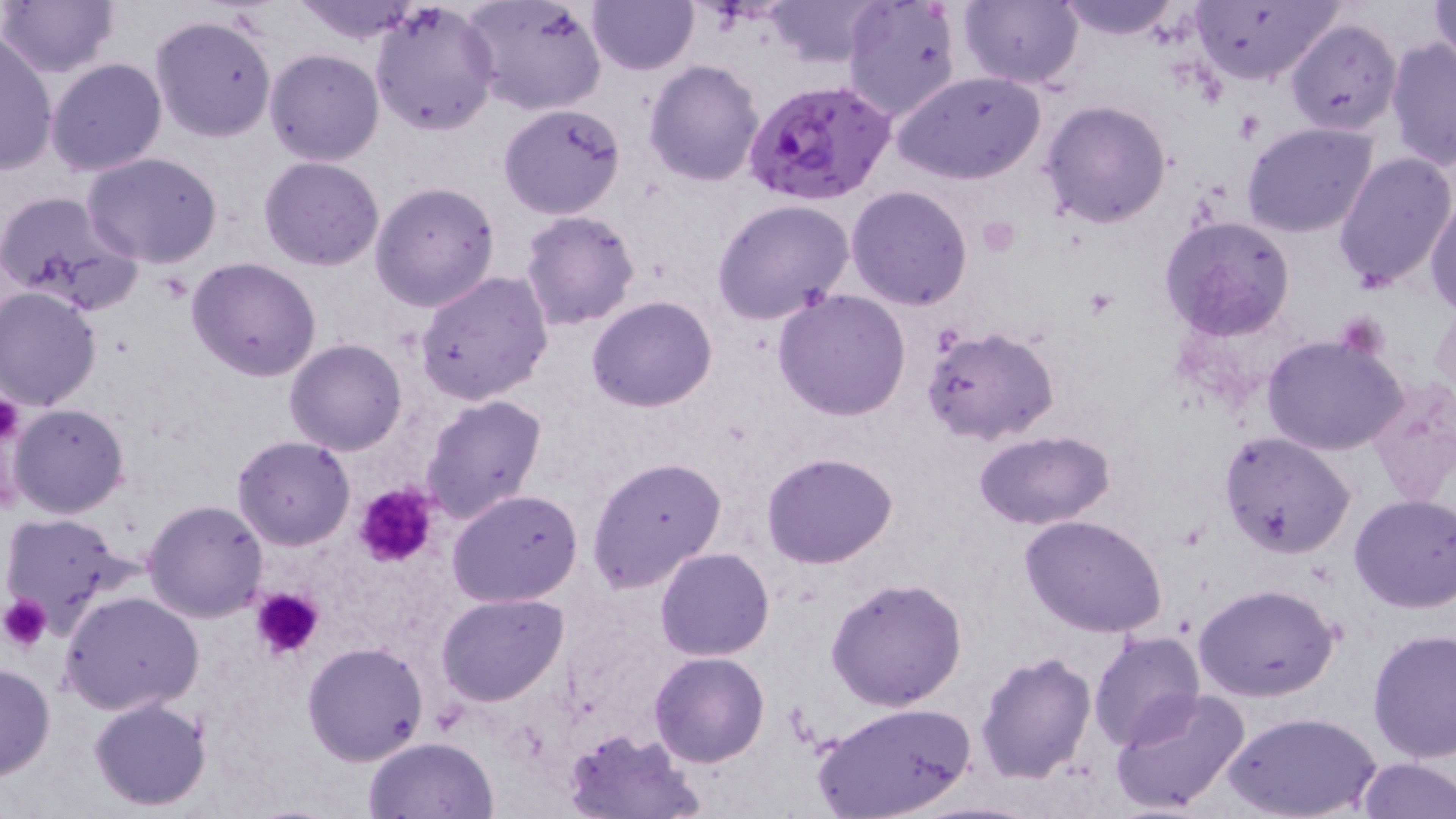
Approximate bounding boxes as named x1/y1/x2/y2 corners in pixels. Plasmodium falciparum-infected red blood cell locations: (x1=742, y1=79, x2=895, y2=208). Platelet locations: (x1=976, y1=214, x2=1017, y2=256), (x1=0, y1=391, x2=26, y2=449), (x1=354, y1=483, x2=439, y2=568), (x1=252, y1=587, x2=323, y2=659), (x1=3, y1=597, x2=52, y2=650). Uninfected red blood cell locations: (x1=0, y1=0, x2=123, y2=80), (x1=292, y1=0, x2=424, y2=44), (x1=370, y1=0, x2=500, y2=138), (x1=763, y1=0, x2=884, y2=68), (x1=958, y1=0, x2=1084, y2=90), (x1=1051, y1=0, x2=1184, y2=41), (x1=1427, y1=0, x2=1456, y2=70), (x1=462, y1=1, x2=607, y2=117), (x1=588, y1=1, x2=698, y2=75), (x1=1188, y1=1, x2=1343, y2=87), (x1=843, y1=3, x2=960, y2=122), (x1=150, y1=14, x2=277, y2=142), (x1=1285, y1=16, x2=1402, y2=135), (x1=1, y1=33, x2=57, y2=174), (x1=1385, y1=40, x2=1456, y2=169), (x1=264, y1=49, x2=383, y2=166), (x1=44, y1=58, x2=166, y2=176), (x1=645, y1=59, x2=766, y2=187), (x1=895, y1=71, x2=1045, y2=185), (x1=1040, y1=98, x2=1171, y2=228), (x1=500, y1=103, x2=626, y2=219), (x1=1242, y1=122, x2=1380, y2=239), (x1=1332, y1=151, x2=1454, y2=292), (x1=81, y1=152, x2=225, y2=269), (x1=259, y1=156, x2=386, y2=271), (x1=369, y1=182, x2=501, y2=312), (x1=847, y1=186, x2=973, y2=310), (x1=0, y1=189, x2=144, y2=314), (x1=1426, y1=196, x2=1456, y2=315), (x1=711, y1=199, x2=855, y2=324), (x1=519, y1=210, x2=641, y2=331), (x1=1161, y1=214, x2=1297, y2=340), (x1=186, y1=257, x2=322, y2=381), (x1=415, y1=271, x2=554, y2=406), (x1=0, y1=285, x2=103, y2=410), (x1=773, y1=290, x2=912, y2=420), (x1=586, y1=295, x2=717, y2=411), (x1=1430, y1=297, x2=1455, y2=412), (x1=922, y1=323, x2=1061, y2=445), (x1=1262, y1=333, x2=1409, y2=457), (x1=285, y1=339, x2=408, y2=455), (x1=1366, y1=376, x2=1456, y2=508), (x1=419, y1=393, x2=549, y2=525), (x1=8, y1=402, x2=131, y2=518), (x1=971, y1=430, x2=1118, y2=527), (x1=1219, y1=431, x2=1355, y2=556), (x1=232, y1=435, x2=356, y2=551), (x1=761, y1=453, x2=898, y2=570), (x1=587, y1=456, x2=727, y2=595), (x1=447, y1=490, x2=585, y2=607), (x1=1349, y1=495, x2=1456, y2=613), (x1=142, y1=498, x2=270, y2=623), (x1=1, y1=512, x2=138, y2=639), (x1=1019, y1=515, x2=1168, y2=637), (x1=654, y1=547, x2=776, y2=661), (x1=825, y1=576, x2=968, y2=711), (x1=1193, y1=582, x2=1340, y2=701), (x1=61, y1=591, x2=205, y2=716), (x1=436, y1=594, x2=569, y2=706), (x1=1368, y1=629, x2=1456, y2=762), (x1=1088, y1=630, x2=1207, y2=752), (x1=302, y1=641, x2=428, y2=767), (x1=649, y1=651, x2=771, y2=768), (x1=977, y1=651, x2=1095, y2=785), (x1=0, y1=663, x2=56, y2=781), (x1=1110, y1=689, x2=1253, y2=816), (x1=87, y1=696, x2=214, y2=810), (x1=811, y1=701, x2=978, y2=819), (x1=1225, y1=711, x2=1379, y2=819), (x1=565, y1=729, x2=705, y2=817), (x1=363, y1=737, x2=499, y2=819), (x1=1354, y1=756, x2=1456, y2=818). Slide-level diagnosis: Plasmodium falciparum. Captured at 1000x magnification. Light microscopy. Image is 1456×819 pixels. Thin blood smear. May-Grünwald-Giemsa stain. Single field of view.